Report the malaria status of this cell.
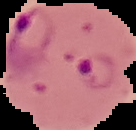
It is parasitized.

Summary:
  - Image type: segmented cell region with the area outside set to black
  - Image size: 136×130 pixels
  - Preparation: thin blood smear